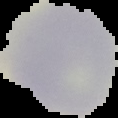

Summary:
  - Result: negative for malaria parasites
  - Preparation: thin blood smear
  - Image size: 118×118 pixels
  - Image type: segmented cell region with the area outside set to black